Assess this cell for malaria.
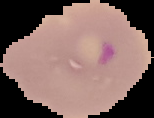
It is parasitized.

Summary:
  - Image type: cell region segmented out of the field of view; surrounding area masked to black
  - Image size: 154×118 pixels
  - Preparation: thin blood film